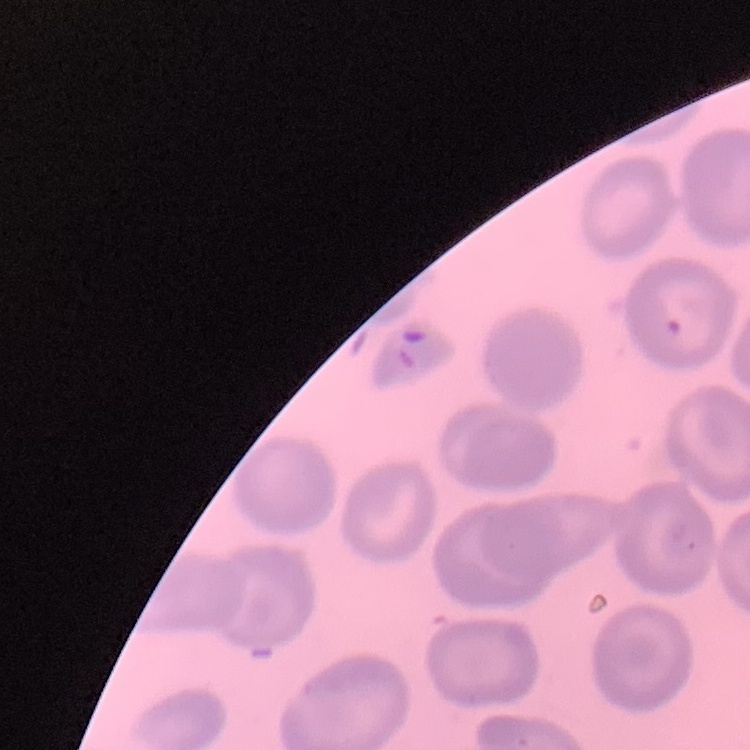
{
  "erythrocyte_morphology": "no rouleaux formation",
  "stain": "Field's or Giemsa",
  "image_type": "square crop of a larger photomicrograph",
  "preparation": "thin blood film"
}